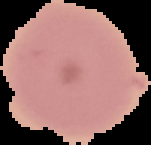

image_size: 151×145 pixels
preparation: thin blood film
image_type: segmented cell region on a black background
malaria_status: uninfected